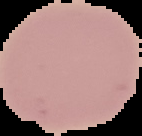
Summary:
  - Image size: 142×136 pixels
  - Preparation: thin blood film
  - Malaria status: uninfected
  - Image type: segmented cell region on a black background